Assess for parasitized red blood cells.
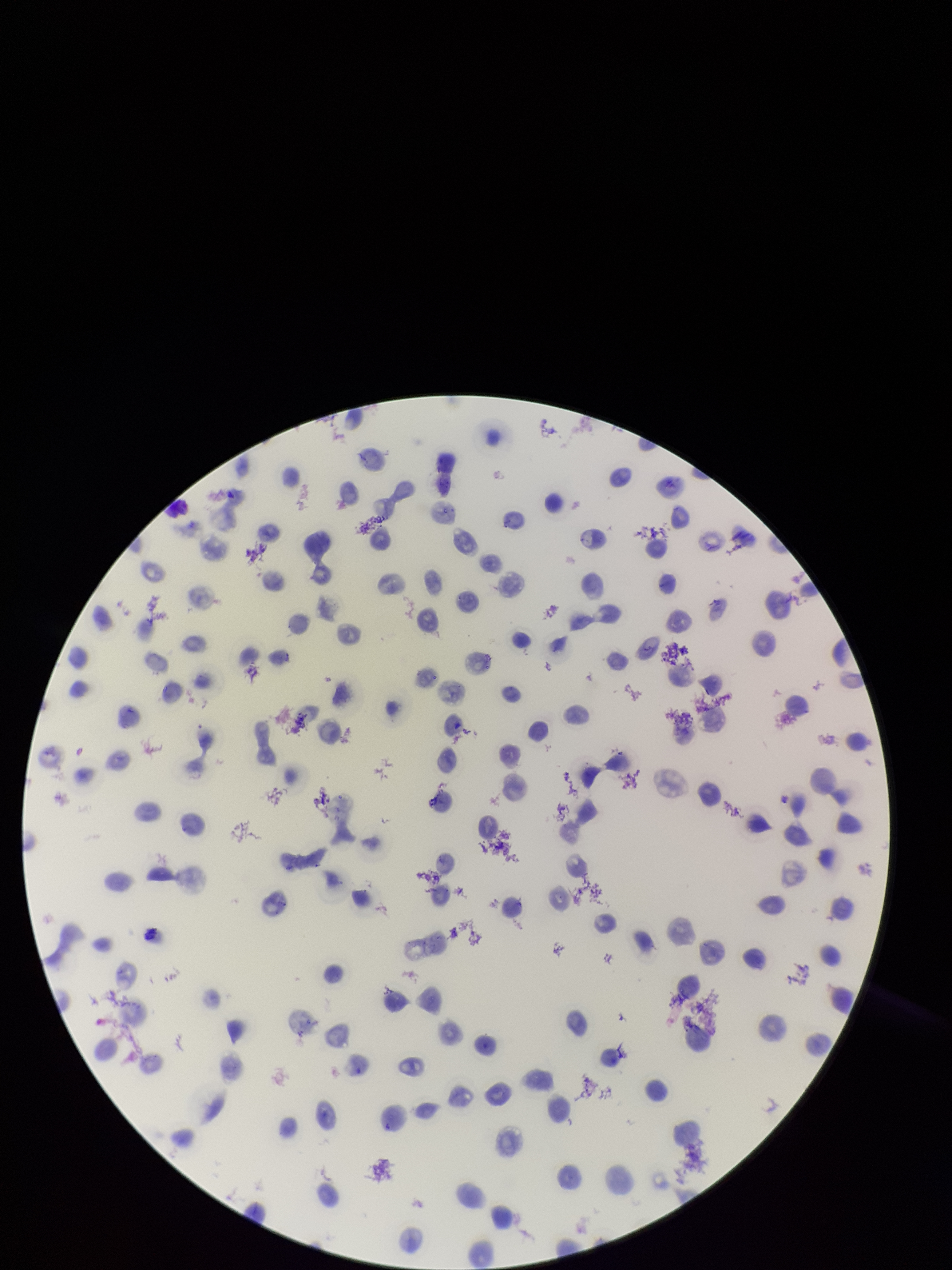
None seen.

Patient malaria status: infected. Photographed through the microscope eyepiece with a smartphone camera. Species reported for this patient: Plasmodium vivax. Single field of view. Giemsa stain. Red blood cell count: 98. Preparation: thin smear. Parasitized red blood cell count: 0. Image is 952×1270 pixels.